Outline each Plasmodium falciparum-infected red blood cell.
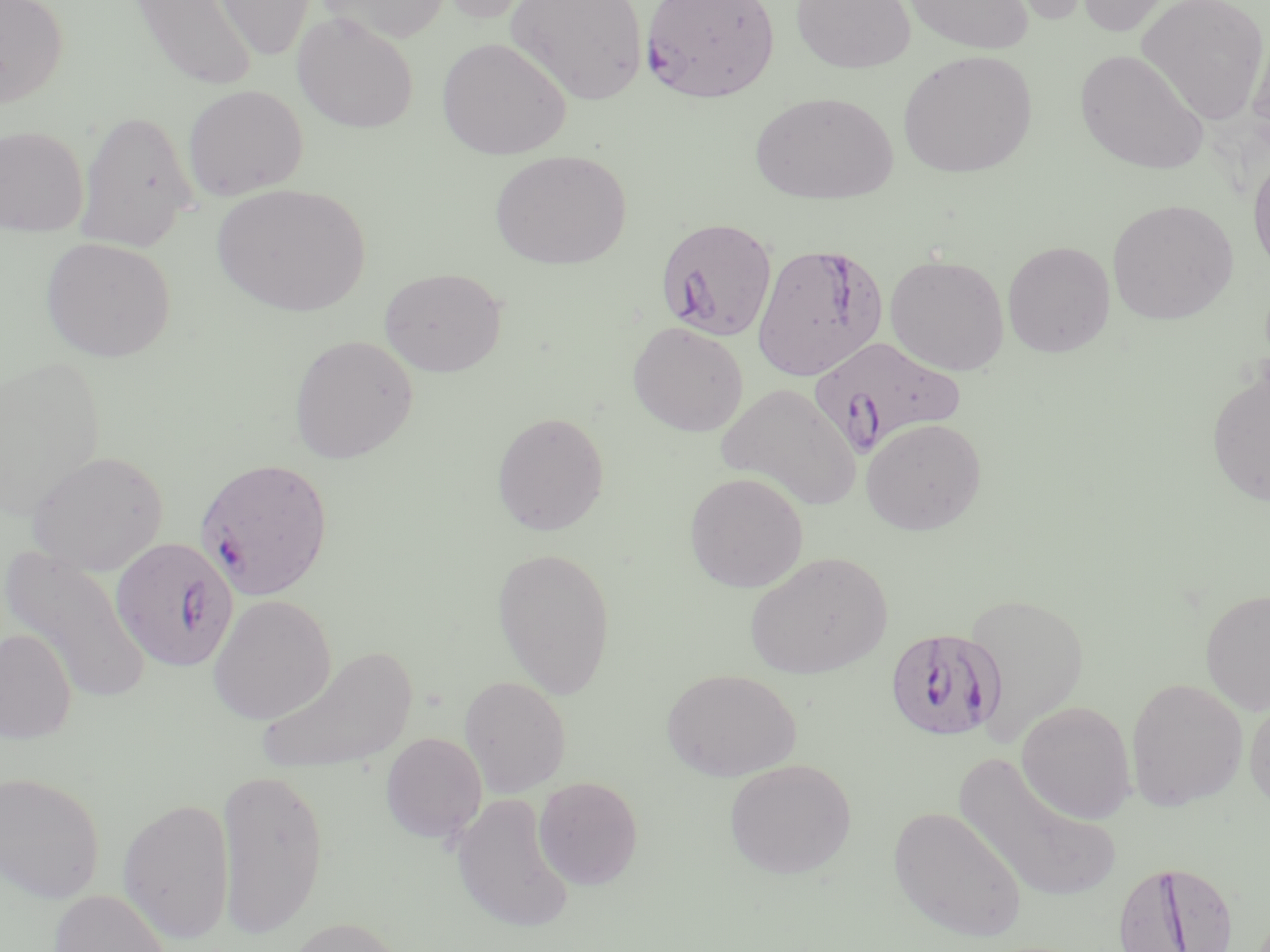

Approximate bounding boxes as (x1, y1, x2, y2) in pixels.
Plasmodium falciparum-infected red blood cells: (640, 0, 781, 103), (655, 217, 778, 342), (752, 242, 889, 382), (810, 336, 963, 458), (195, 457, 335, 601), (110, 536, 238, 673), (885, 627, 1007, 742), (1112, 859, 1240, 952).

slide-level diagnosis = Plasmodium falciparum
modality = light microscopy
field of view = one of a larger specimen
image size = 1270×952 pixels
magnification = 1000x
uninfected red blood cell locations = approximate bounding boxes as (x1, y1, x2, y2) in pixels: (0, 0, 69, 108), (212, 0, 316, 62), (315, 0, 450, 43), (432, 0, 546, 24), (507, 0, 648, 106), (791, 0, 916, 73), (899, 0, 1035, 55), (989, 0, 1098, 26), (1071, 0, 1180, 36), (1136, 0, 1270, 125), (129, 1, 258, 93), (292, 12, 419, 134), (1248, 23, 1270, 151), (437, 36, 571, 159), (1074, 49, 1209, 176), (897, 50, 1037, 178), (182, 84, 308, 200), (749, 91, 897, 205), (75, 110, 198, 252), (0, 125, 89, 236), (489, 149, 632, 270), (1248, 152, 1270, 277), (212, 183, 372, 317), (1107, 198, 1239, 325), (41, 237, 176, 363), (1002, 241, 1116, 357), (885, 254, 1010, 375), (380, 267, 507, 377), (627, 321, 748, 437), (288, 334, 418, 464), (0, 356, 106, 520), (1206, 367, 1270, 508), (715, 383, 862, 512), (492, 411, 610, 536), (861, 417, 986, 535), (28, 450, 169, 575), (684, 472, 809, 592), (1, 545, 153, 704), (492, 546, 616, 699), (744, 551, 892, 680), (1200, 589, 1270, 716), (963, 592, 1090, 745), (207, 594, 336, 725), (0, 628, 77, 744), (256, 645, 418, 778), (662, 668, 801, 781), (459, 675, 571, 797), (1126, 678, 1248, 811), (1244, 695, 1270, 814), (1016, 701, 1136, 824), (380, 733, 487, 844), (952, 751, 1121, 906), (724, 758, 857, 879), (215, 765, 329, 940), (0, 770, 105, 903), (533, 776, 643, 890), (450, 792, 574, 933), (118, 796, 235, 944), (888, 805, 1027, 943), (48, 888, 173, 952), (283, 916, 410, 952)
preparation = thin blood film
stain = May-Grünwald-Giemsa